Assess this cell for malaria.
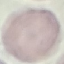

It is uninfected.

image type = automatically extracted cell patch, resized to 64 × 64 pixels
preparation = thin blood smear
capture = smartphone camera at the microscope eyepiece
stain = Giemsa